Point out each Plasmodium parasite.
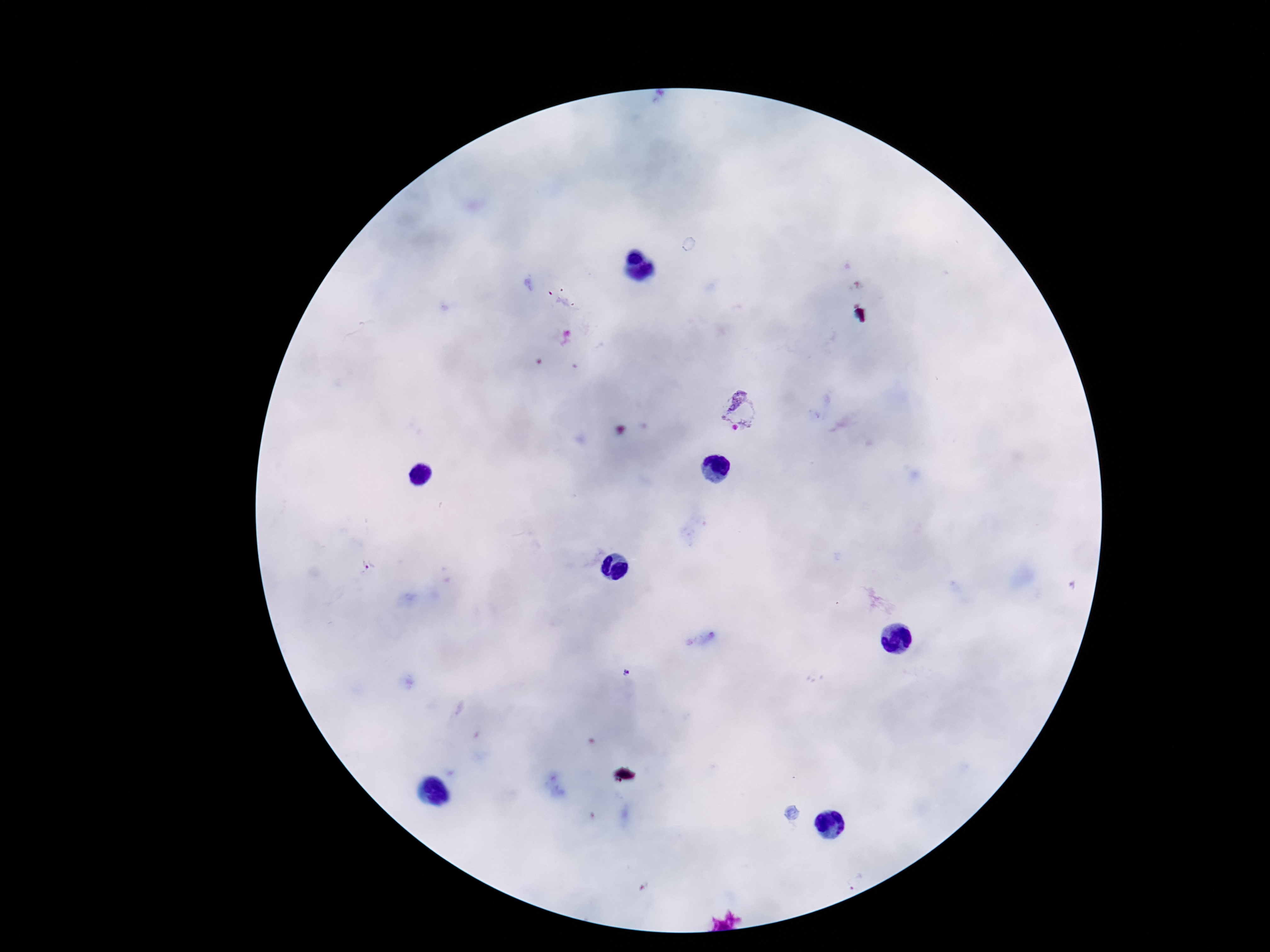
Approximate object centers, in pixels from the top-left corner.
Plasmodium parasites: (x=742, y=411), (x=369, y=565).

Summary:
  - Image size: 1270×952 pixels
  - Magnification: 100x
  - Preparation: thick peripheral-blood smear
  - Field of view: single
  - Stain: Giemsa
  - Patient malaria status: positive
  - Capture: smartphone camera through the microscope eyepiece